Identify the parasite.
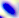

This is Toxoplasma gondii.

Summary:
  - Magnification: 400x
  - Modality: micrograph